Look for Plasmodium parasites.
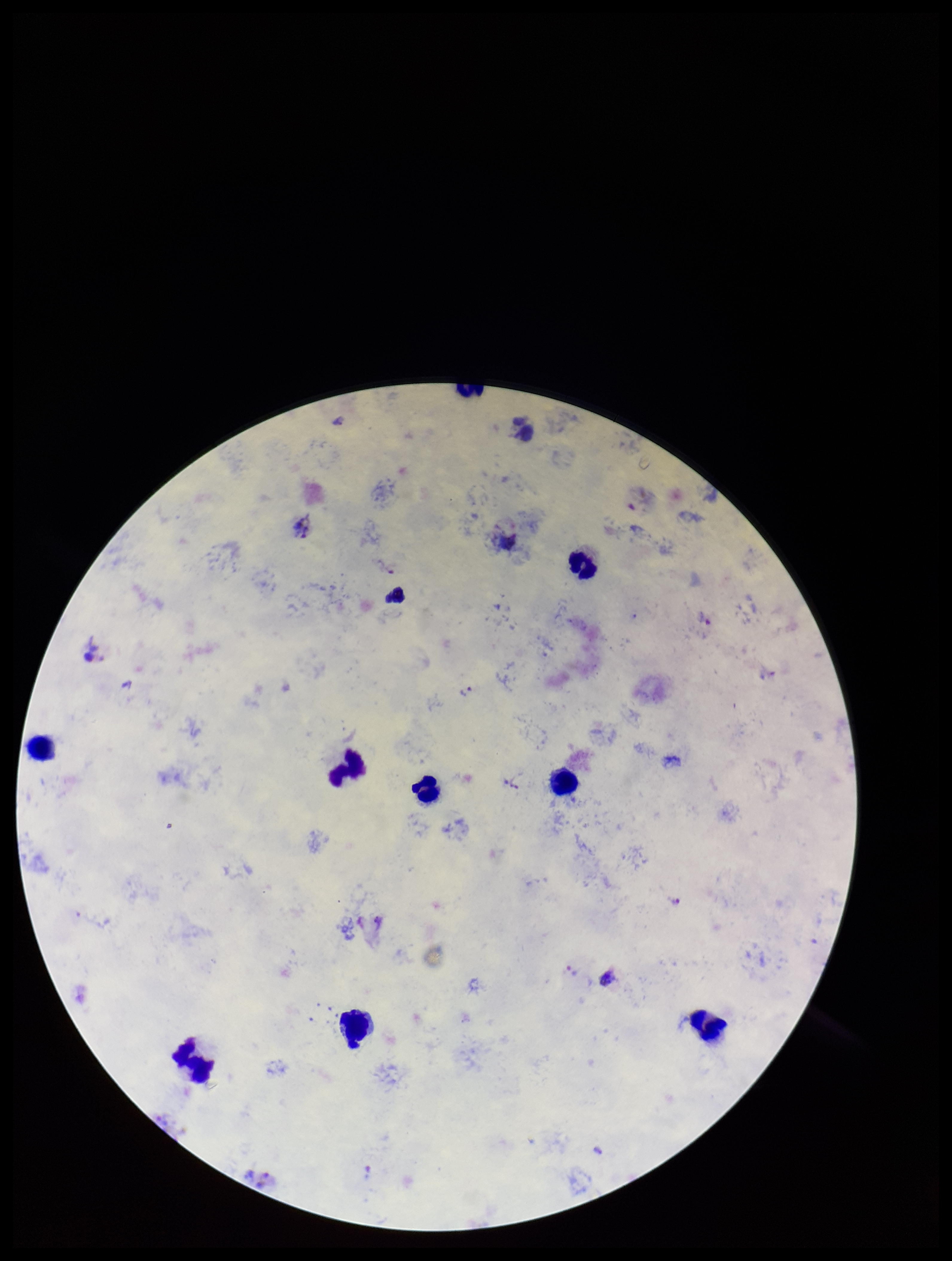
Identified.

Summary:
  - Capture: smartphone photograph through the microscope eyepiece
  - Leukocyte count: 9
  - Species reported for this patient: Plasmodium vivax
  - Patient malaria status: positive
  - Parasite count: 3
  - Image size: 952×1261 pixels
  - Preparation: thick smear
  - Field of view: one from this slide
  - Stain: Giemsa